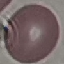

Malaria status: uninfected. Cell patch, automatically extracted from a larger field of view and resized to 64 × 64 pixels. Photographed with a smartphone camera at the microscope eyepiece. Thin blood smear. Giemsa stain.